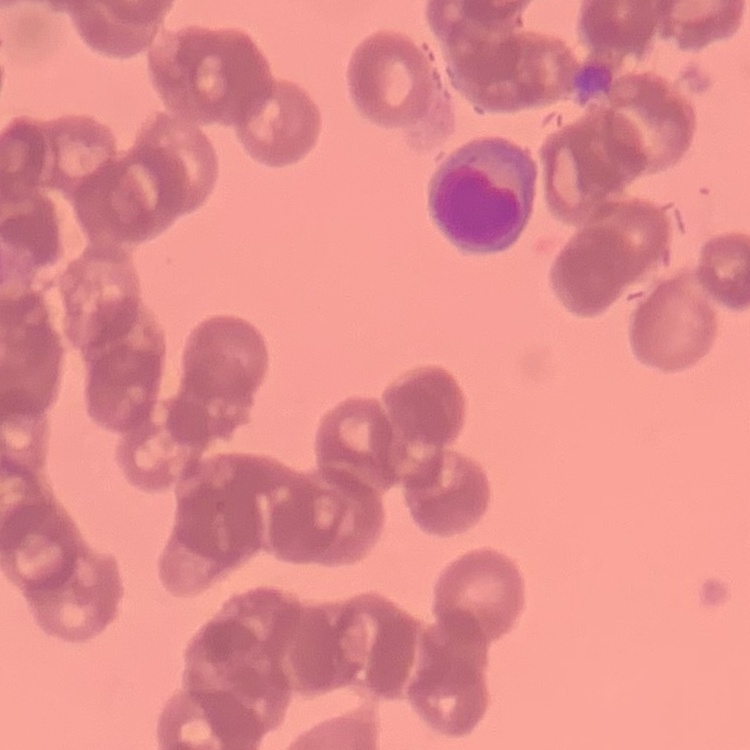
{
  "red_blood_cell_morphology": "rouleaux formation",
  "image_type": "one tile cut from a larger photomicrograph",
  "preparation": "thin blood smear",
  "stain": "Field's or Giemsa"
}